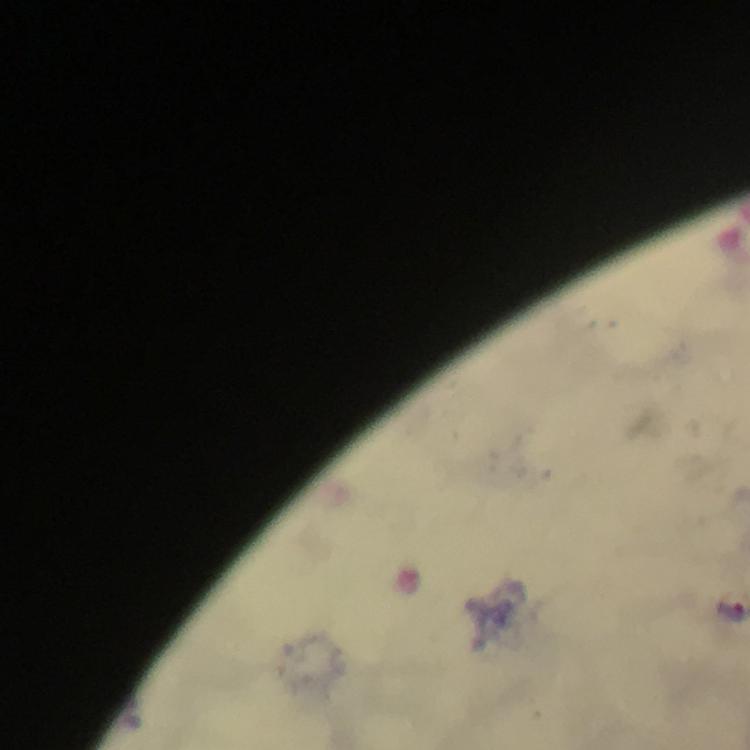

immersion oil = applied
Plasmodium parasite locations = approximate centers as {x, y} in pixels: {729, 610}
preparation = thick blood film
cropped from = one field of view
image size = 750×750 pixels
magnification = 100x
stain = Giemsa
context = from a malaria diagnostic workup
capture = smartphone mounted on the microscope